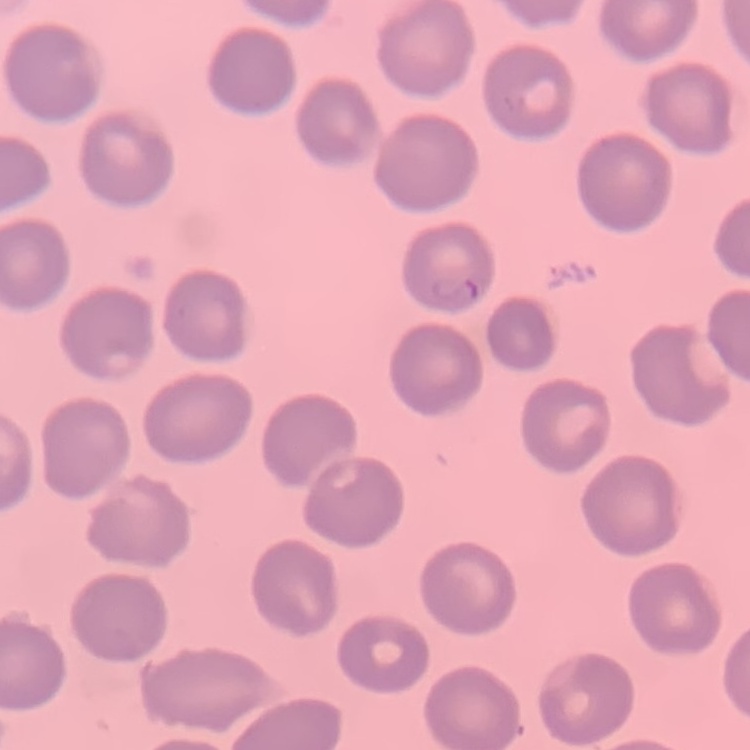

The erythrocytes exhibit no rouleaux formation. Thin blood smear. Stained with either Field's or Giemsa. Square crop of a larger photomicrograph.